Locate and identify every blood parasite.
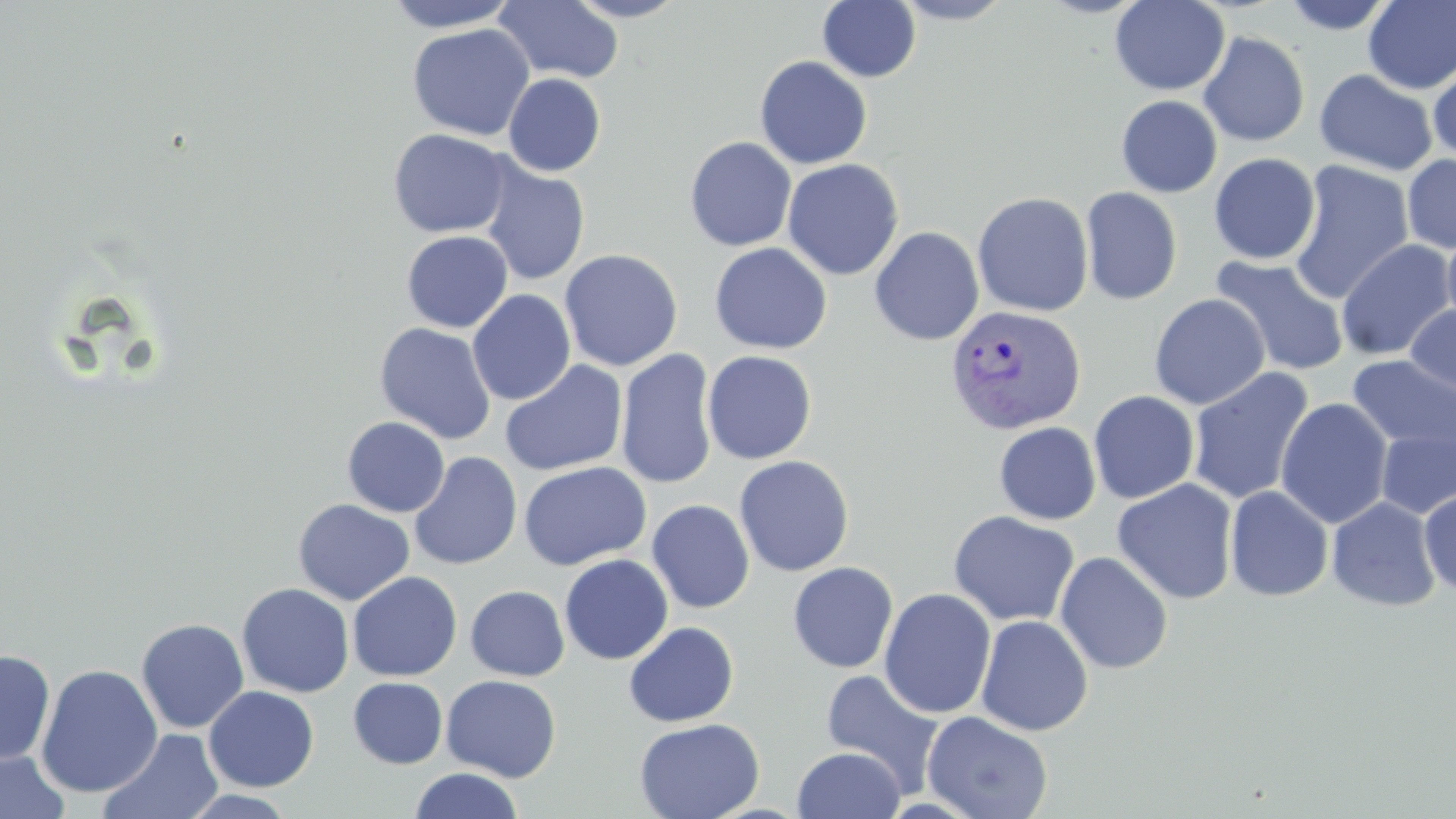
Approximate bounding boxes as (x1,y1)-(x2,y2) corner pairs in pixels.
Plasmodium vivax-infected red blood cells: (945,304)-(1086,435).
No Plasmodium falciparum, Plasmodium ovale, Plasmodium malariae, Babesia divergens, or Trypanosoma brucei observed.

Summary:
  - Uninfected red blood cell locations: (381,0)-(522,32), (565,0)-(688,22), (817,0)-(922,82), (892,0)-(1014,25), (1109,0)-(1230,96), (1280,0)-(1398,35), (493,1)-(625,84), (1362,1)-(1456,94), (407,23)-(535,141), (1198,31)-(1310,146), (754,56)-(873,169), (1428,62)-(1456,165), (1314,69)-(1438,177), (503,73)-(606,176), (1116,95)-(1222,198), (388,129)-(511,238), (684,136)-(797,251), (1209,153)-(1320,265), (1402,153)-(1456,254), (782,159)-(904,280), (1288,159)-(1414,303), (479,162)-(590,286), (1080,187)-(1182,305), (972,191)-(1094,317), (1442,224)-(1456,331), (869,226)-(984,345), (401,230)-(513,333), (1336,239)-(1455,361), (709,242)-(832,354), (559,249)-(683,372), (1210,256)-(1349,376), (467,289)-(576,405), (1149,293)-(1270,410), (1404,303)-(1456,400), (374,322)-(497,445), (615,348)-(718,490), (701,350)-(817,465), (1347,355)-(1456,455), (500,360)-(628,477), (1187,367)-(1314,505), (1089,390)-(1200,504), (1276,397)-(1393,528), (342,416)-(450,517), (994,422)-(1101,524), (1376,426)-(1456,519), (409,452)-(522,571), (734,455)-(854,576), (518,461)-(651,570), (1112,479)-(1239,604), (1225,485)-(1334,602), (1419,489)-(1456,596), (1327,496)-(1441,611), (293,498)-(414,606), (647,499)-(754,613), (947,511)-(1080,627), (1054,551)-(1173,674), (559,554)-(674,664), (787,561)-(898,673), (348,571)-(462,681), (237,582)-(355,698), (465,585)-(569,681), (879,588)-(996,718), (975,615)-(1093,736), (136,618)-(249,734), (623,621)-(739,727), (0,649)-(56,766), (35,664)-(163,798), (820,668)-(946,797), (441,674)-(561,782), (348,677)-(448,769), (204,685)-(319,791), (922,710)-(1054,819), (634,716)-(764,819), (99,728)-(224,819), (793,746)-(906,819), (0,748)-(70,819), (408,768)-(524,819), (178,789)-(299,819)
  - Slide-level diagnosis: Plasmodium vivax
  - Modality: optical microscopy
  - Stain: May-Grünwald-Giemsa
  - Magnification: 1000x
  - Image size: 1456×819 pixels
  - Field of view: single
  - Preparation: thin blood smear